Assess this cell for malaria.
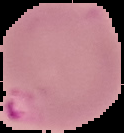

Parasitized.

From a thin blood smear. The area outside the segmented cell region is set to black. Image is 124×133 pixels.